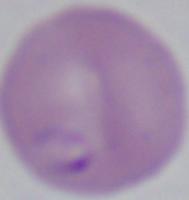
Summary:
  - Magnification: 1000x
  - Modality: photomicrograph
  - Identification: Babesia